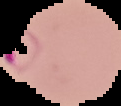

result = Plasmodium parasites detected
image size = 121×106 pixels
image type = cell region segmented out of the field of view; surrounding area masked to black
preparation = thin blood film